Give the position of every malaria parasite.
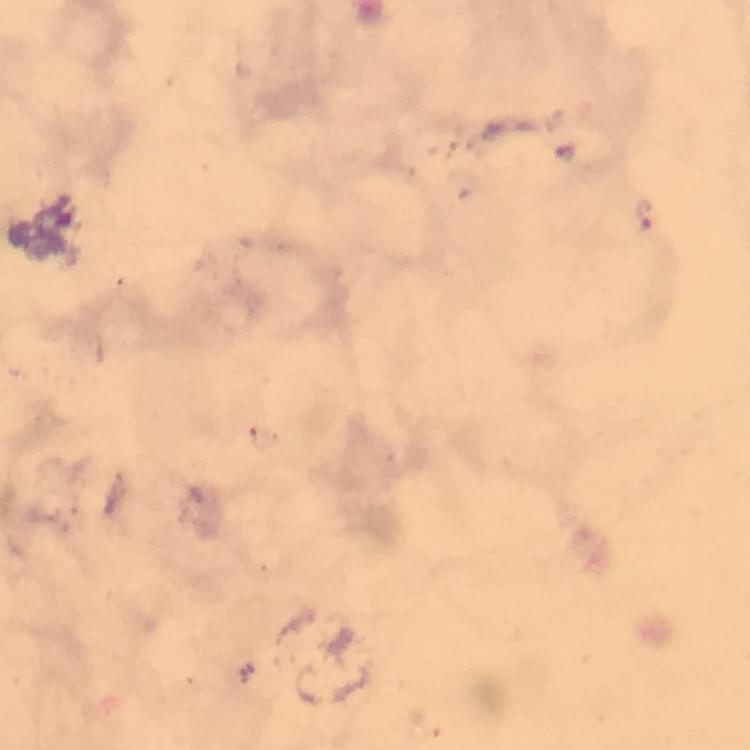
Approximate centers as {x, y} in pixels.
Malaria parasites: {563, 151}, {645, 215}.

{
  "preparation": "thick blood film",
  "immersion_oil": "applied",
  "image_size": "750×750 pixels",
  "context": "from a malaria diagnostic workup",
  "stain": "Giemsa",
  "magnification": "100x",
  "cropped_from": "one field of view",
  "capture": "smartphone mounted on the microscope"
}